Evaluate for malaria.
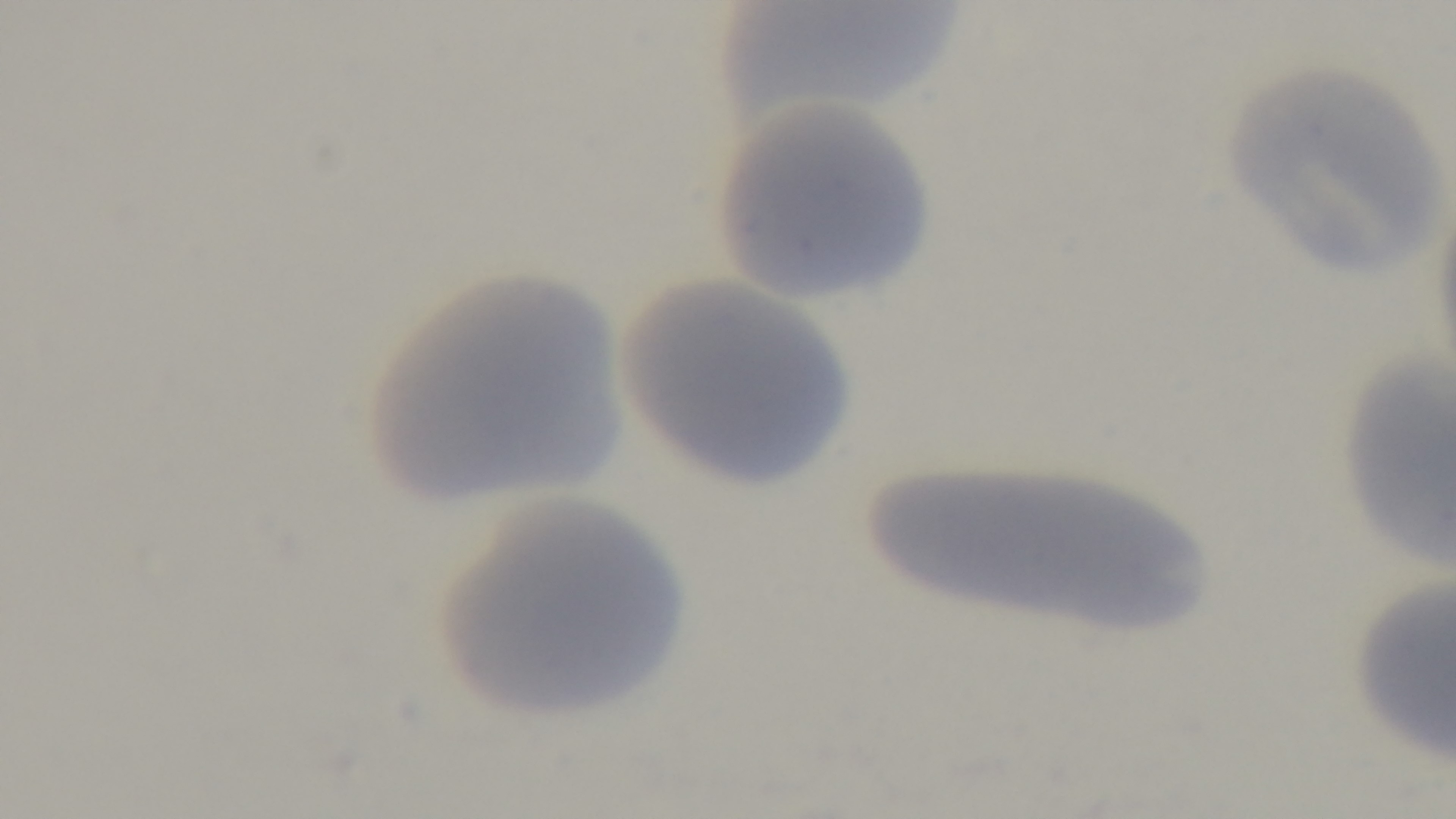

Uninfected.

Summary:
  - Modality: light microscopy
  - Objective: 100x oil immersion
  - Field of view: single
  - Preparation: thin blood film
  - Capture: mounted 4K digital camera
  - Stain: Giemsa